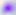

Summary:
  - Identification: Toxoplasma gondii
  - Modality: photomicrograph
  - Magnification: 400x